Report the malaria status of this cell.
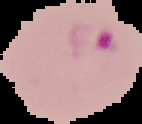
It is parasitized.

Image is 142×124 pixels. Cell region segmented out of the field of view; the surrounding area is masked to black. From a thin blood film.